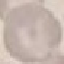
Summary:
  - Malaria status: uninfected
  - Preparation: thin blood film
  - Capture: smartphone camera at the microscope eyepiece
  - Stain: Giemsa
  - Image type: automatically extracted cell patch, resized to 64 × 64 pixels